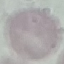

malaria status = uninfected
image type = cell patch, automatically extracted from a larger field of view and resized to 64 × 64 pixels
capture = smartphone through the microscope eyepiece
stain = Giemsa
preparation = thin blood film